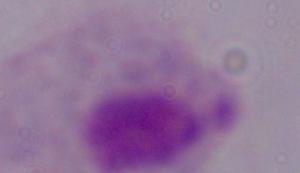
magnification: 1000x
modality: photomicrograph
identification: trichomonad